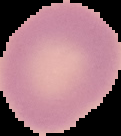
image size = 121×136 pixels
preparation = thin blood film
image type = segmented cell region on a black background
malaria status = uninfected